Name the parasite shown.
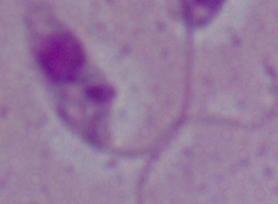

Leishmania.

Micrograph. 1000x magnification.